Report the malaria status of this cell.
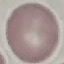
Uninfected.

Photographed with a smartphone camera at the microscope eyepiece. Giemsa stain. Thin blood smear. Automatically extracted cell patch, resized to 64 × 64 pixels.